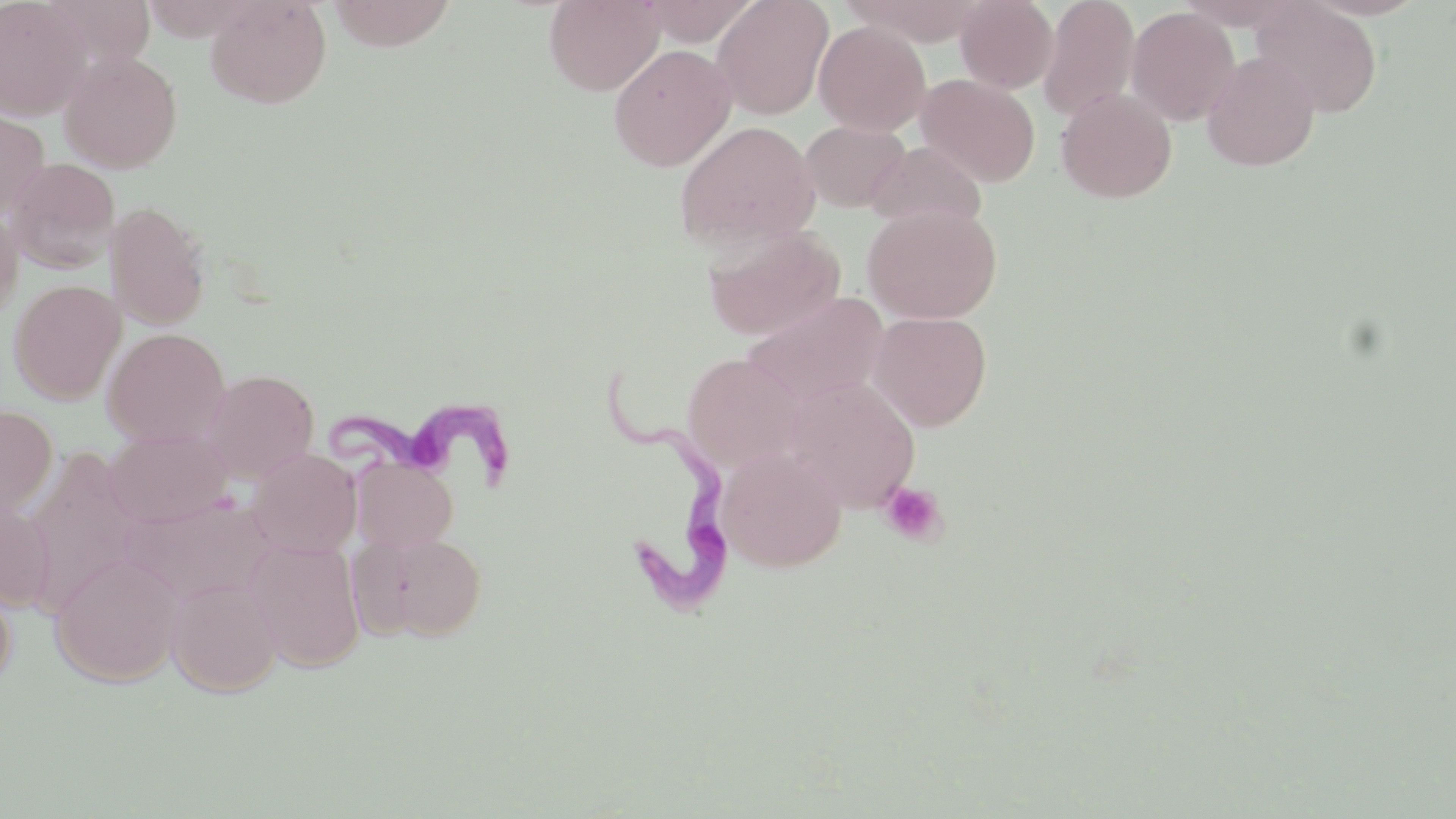

Approximate bounding boxes as (x1,y1)-(x2,y2) corner pairs in pixels. Trypanosoma brucei locations: (602,365)-(729,625), (326,389)-(521,487). Platelet locations: (878,481)-(947,546). Uninfected red blood cell locations: (0,0)-(91,121), (205,0)-(332,109), (325,0)-(458,51), (544,0)-(664,95), (634,0)-(761,46), (711,0)-(834,119), (841,0)-(991,46), (955,0)-(1058,93), (1037,0)-(1140,123), (1250,1)-(1383,117), (1126,6)-(1240,126), (814,20)-(932,137), (608,43)-(737,172), (58,50)-(183,173), (1202,51)-(1320,171), (916,73)-(1041,187), (1055,86)-(1177,203), (0,107)-(50,217), (674,120)-(820,250), (799,120)-(910,212), (866,140)-(987,232), (5,157)-(120,274), (104,201)-(212,330), (863,204)-(1003,324), (0,205)-(23,323), (702,225)-(846,341), (8,280)-(126,404), (742,291)-(890,407), (869,311)-(992,431), (102,327)-(230,447), (682,353)-(804,472), (201,369)-(319,483), (785,377)-(921,511), (0,404)-(58,519), (104,427)-(233,528), (716,445)-(847,572), (24,446)-(143,613), (246,448)-(362,559), (352,458)-(458,553), (121,494)-(273,606), (0,501)-(55,613), (357,530)-(488,642), (245,536)-(366,672), (50,553)-(184,687), (0,573)-(17,690), (167,577)-(281,698). Slide-level diagnosis: Trypanosoma brucei. Image is 1456×819 pixels. May-Grünwald-Giemsa-stained preparation. 1000x magnification. Thin blood smear. Single field of view. Optical microscopy.